Name the parasite shown.
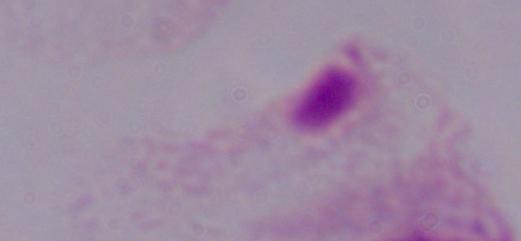
This is a trichomonad.

Summary:
  - Magnification: 1000x
  - Modality: micrograph